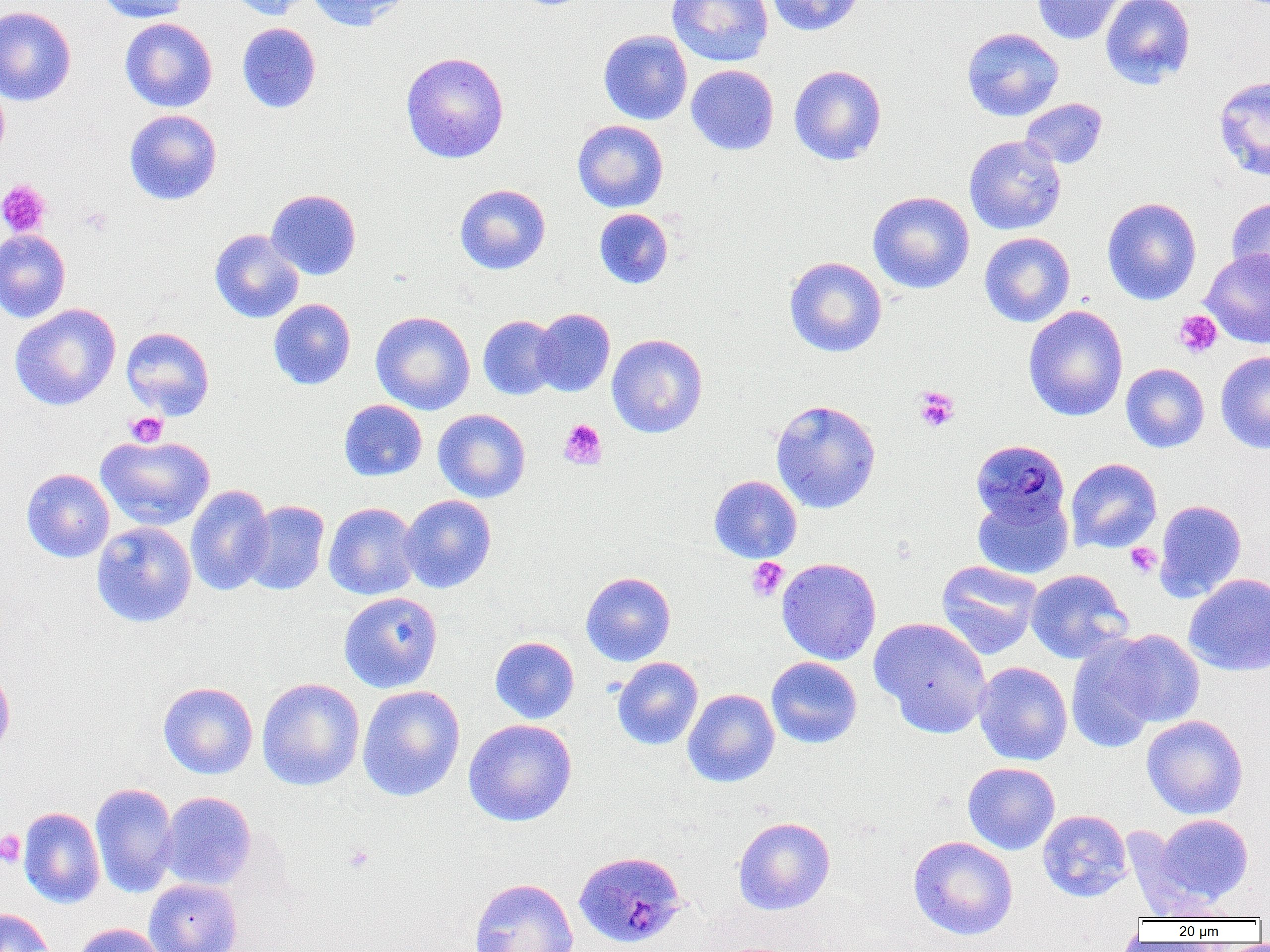
Summary:
  - Coordinate format: approximate bounding boxes as (x1, y1, x2, y2) in pixels
  - Platelet locations: (0, 179, 52, 236), (79, 206, 113, 237), (1174, 310, 1222, 358), (913, 386, 960, 432), (125, 412, 168, 447), (559, 419, 607, 470), (1125, 542, 1161, 578), (747, 557, 788, 602), (0, 830, 26, 867), (343, 844, 375, 873)
  - Uninfected red blood cell locations: (95, 0, 191, 23), (224, 0, 313, 20), (306, 0, 410, 31), (666, 0, 774, 67), (765, 0, 866, 36), (1031, 0, 1126, 45), (1100, 0, 1195, 89), (0, 5, 77, 106), (119, 18, 217, 112), (237, 22, 321, 114), (962, 27, 1064, 122), (598, 29, 693, 125), (400, 51, 510, 163), (686, 64, 778, 155), (788, 65, 887, 165), (1213, 75, 1270, 181), (0, 81, 9, 167), (1020, 98, 1108, 169), (124, 109, 222, 205), (572, 120, 668, 212), (964, 135, 1066, 235), (454, 184, 551, 275), (266, 189, 362, 280), (867, 191, 974, 294), (1101, 196, 1203, 305), (1226, 196, 1270, 286), (594, 208, 673, 289), (209, 228, 305, 324), (0, 229, 71, 323), (979, 232, 1075, 327), (1200, 249, 1270, 348), (784, 256, 887, 357), (268, 298, 356, 389), (9, 304, 121, 411), (1023, 306, 1128, 421), (531, 308, 615, 397), (371, 311, 476, 415), (478, 315, 562, 400), (121, 327, 215, 419), (607, 333, 708, 438), (1216, 350, 1270, 454), (1120, 363, 1210, 452), (339, 399, 427, 481), (770, 399, 882, 514), (433, 408, 531, 503), (95, 434, 216, 531), (1065, 458, 1162, 553), (21, 468, 115, 563), (709, 474, 802, 563), (185, 484, 275, 595), (972, 492, 1074, 579), (398, 494, 497, 593), (1154, 499, 1247, 602), (241, 500, 330, 595), (323, 502, 421, 601), (91, 521, 197, 627), (776, 557, 882, 665), (935, 560, 1043, 659), (1025, 569, 1133, 663), (581, 571, 676, 666), (1184, 573, 1270, 676), (338, 591, 443, 693), (869, 616, 993, 738), (1103, 629, 1205, 729), (1066, 635, 1164, 753), (489, 636, 580, 723), (766, 656, 862, 749), (612, 657, 703, 750), (0, 661, 15, 762), (973, 661, 1073, 765), (256, 677, 365, 791), (158, 681, 258, 779), (357, 685, 465, 801), (683, 688, 780, 787), (1142, 715, 1248, 819), (463, 719, 578, 826), (963, 762, 1060, 854), (90, 782, 179, 898), (160, 791, 256, 890), (19, 807, 105, 909), (1037, 810, 1132, 902), (1154, 814, 1253, 905), (733, 816, 836, 915), (1122, 825, 1218, 920), (908, 836, 1018, 940), (144, 878, 242, 952), (470, 878, 578, 952), (0, 908, 55, 952), (70, 922, 165, 952)
  - Plasmodium malariae-infected red blood cell locations: (971, 439, 1070, 526), (573, 850, 687, 949)
  - Slide-level diagnosis: Plasmodium malariae
  - Preparation: thin blood smear
  - Field of view: one of a larger specimen
  - Modality: optical microscopy
  - Image size: 1270×952 pixels
  - Magnification: 1000x